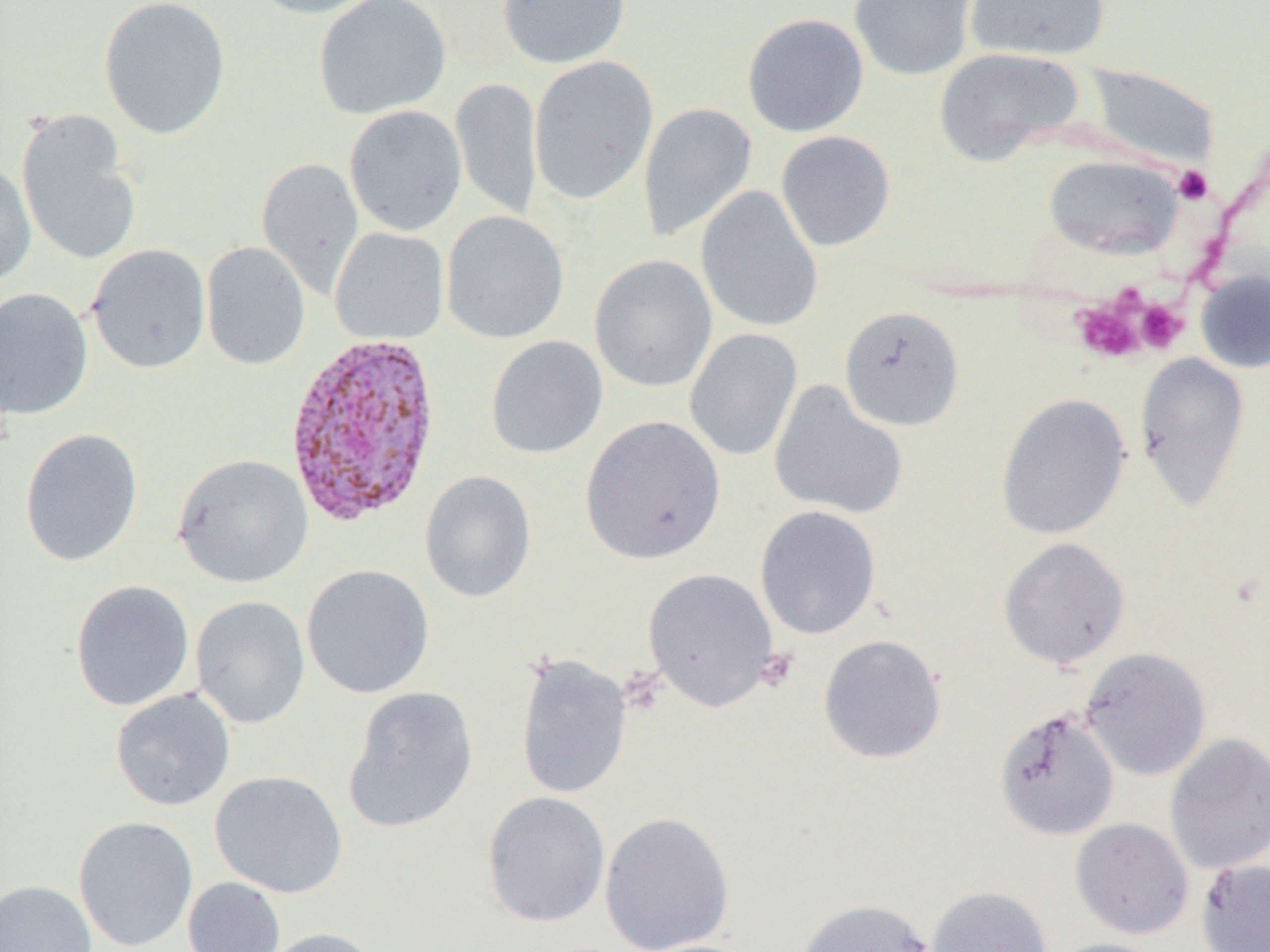

slide-level diagnosis = Plasmodium vivax
modality = light microscopy
field of view = single
preparation = thin blood smear
Plasmodium vivax-infected red blood cell locations = approximate bounding boxes as named x1/y1/x2/y2 corners in pixels: (x1=283, y1=331, x2=444, y2=527)
platelet locations = approximate bounding boxes as named x1/y1/x2/y2 corners in pixels: (x1=1172, y1=165, x2=1213, y2=205), (x1=1071, y1=298, x2=1146, y2=363), (x1=1134, y1=299, x2=1189, y2=354), (x1=755, y1=648, x2=799, y2=691)
image size = 1270×952 pixels
magnification = 1000x
uninfected red blood cell locations = approximate bounding boxes as named x1/y1/x2/y2 corners in pixels: (x1=98, y1=0, x2=231, y2=140), (x1=244, y1=0, x2=385, y2=19), (x1=313, y1=0, x2=451, y2=119), (x1=497, y1=0, x2=631, y2=69), (x1=849, y1=0, x2=978, y2=81), (x1=964, y1=0, x2=1111, y2=62), (x1=742, y1=12, x2=869, y2=137), (x1=934, y1=47, x2=1083, y2=167), (x1=528, y1=55, x2=659, y2=206), (x1=1082, y1=63, x2=1219, y2=169), (x1=450, y1=77, x2=543, y2=221), (x1=637, y1=102, x2=757, y2=243), (x1=344, y1=104, x2=467, y2=236), (x1=16, y1=108, x2=142, y2=267), (x1=776, y1=131, x2=895, y2=252), (x1=1044, y1=154, x2=1184, y2=260), (x1=256, y1=157, x2=364, y2=299), (x1=0, y1=160, x2=36, y2=285), (x1=695, y1=185, x2=824, y2=333), (x1=441, y1=210, x2=569, y2=344), (x1=329, y1=227, x2=449, y2=345), (x1=201, y1=241, x2=310, y2=370), (x1=85, y1=243, x2=211, y2=374), (x1=589, y1=254, x2=718, y2=393), (x1=1195, y1=268, x2=1270, y2=373), (x1=0, y1=287, x2=94, y2=419), (x1=839, y1=305, x2=965, y2=431), (x1=685, y1=328, x2=802, y2=461), (x1=485, y1=335, x2=608, y2=459), (x1=1134, y1=352, x2=1251, y2=512), (x1=769, y1=380, x2=907, y2=520), (x1=996, y1=393, x2=1131, y2=540), (x1=580, y1=413, x2=726, y2=564), (x1=20, y1=428, x2=143, y2=567), (x1=173, y1=453, x2=314, y2=588), (x1=419, y1=470, x2=537, y2=603), (x1=755, y1=505, x2=881, y2=640), (x1=998, y1=537, x2=1130, y2=669), (x1=301, y1=563, x2=435, y2=699), (x1=642, y1=568, x2=780, y2=711), (x1=69, y1=580, x2=195, y2=713), (x1=190, y1=595, x2=311, y2=728), (x1=818, y1=634, x2=946, y2=764), (x1=1079, y1=647, x2=1211, y2=781), (x1=514, y1=653, x2=632, y2=800), (x1=342, y1=687, x2=479, y2=834), (x1=110, y1=688, x2=235, y2=811), (x1=994, y1=707, x2=1120, y2=841), (x1=1165, y1=733, x2=1270, y2=875), (x1=209, y1=770, x2=348, y2=898), (x1=481, y1=791, x2=611, y2=928), (x1=599, y1=811, x2=735, y2=952), (x1=73, y1=815, x2=199, y2=952), (x1=1070, y1=817, x2=1194, y2=939), (x1=1196, y1=858, x2=1270, y2=952), (x1=182, y1=877, x2=286, y2=952), (x1=0, y1=879, x2=97, y2=952), (x1=926, y1=885, x2=1052, y2=952), (x1=795, y1=898, x2=935, y2=952), (x1=259, y1=927, x2=383, y2=952), (x1=1046, y1=938, x2=1168, y2=952)